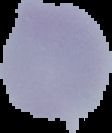
Summary:
  - Image size: 112×133 pixels
  - Image type: segmented cell region on a black background
  - Result: no malaria parasites detected
  - Preparation: thin blood film